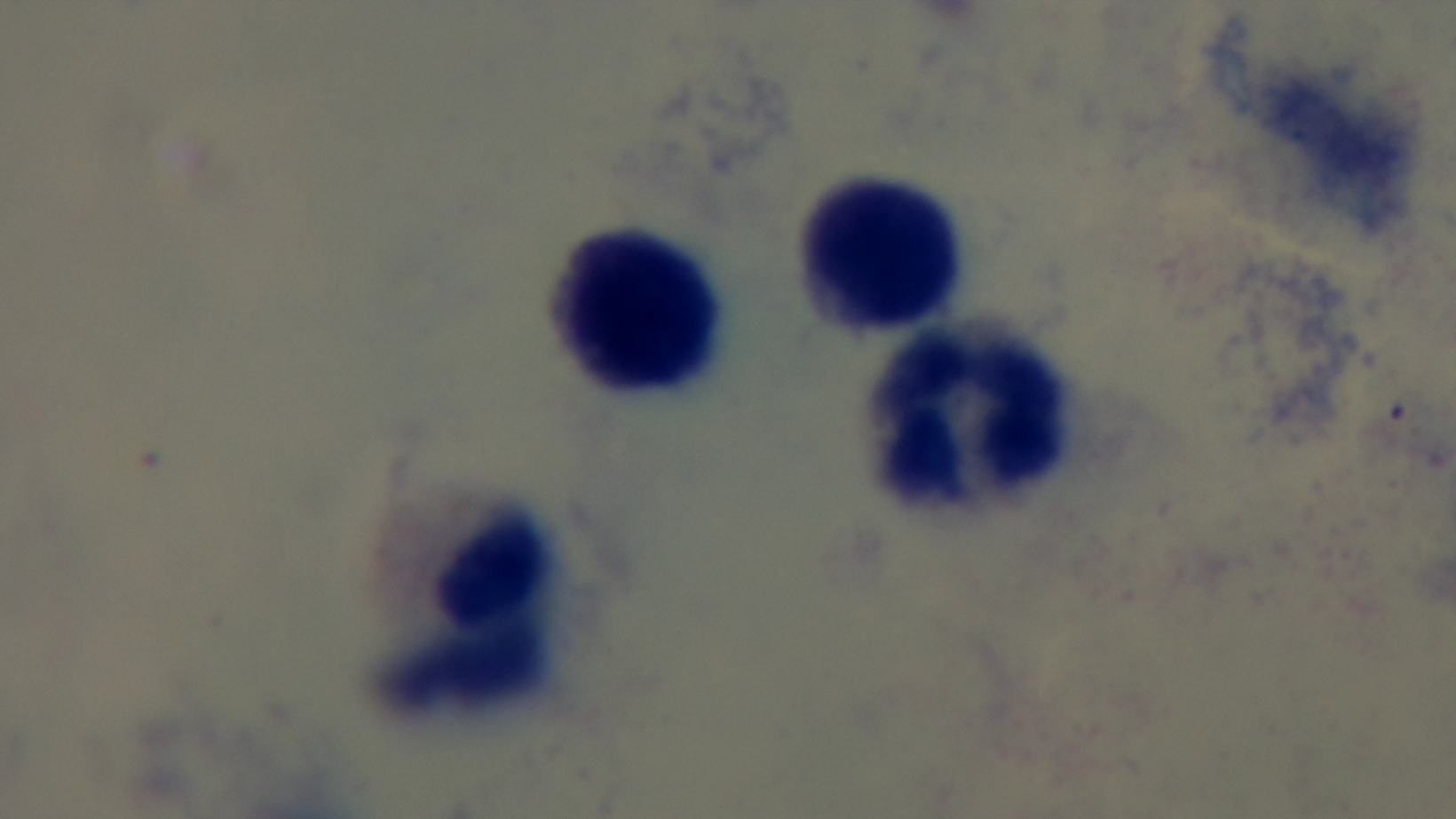
Summary:
  - Malaria status: uninfected
  - Objective: 100x oil immersion
  - Stain: Giemsa
  - Field of view: single
  - Capture: mounted 4K digital camera
  - Preparation: thick smear
  - Modality: light microscopy